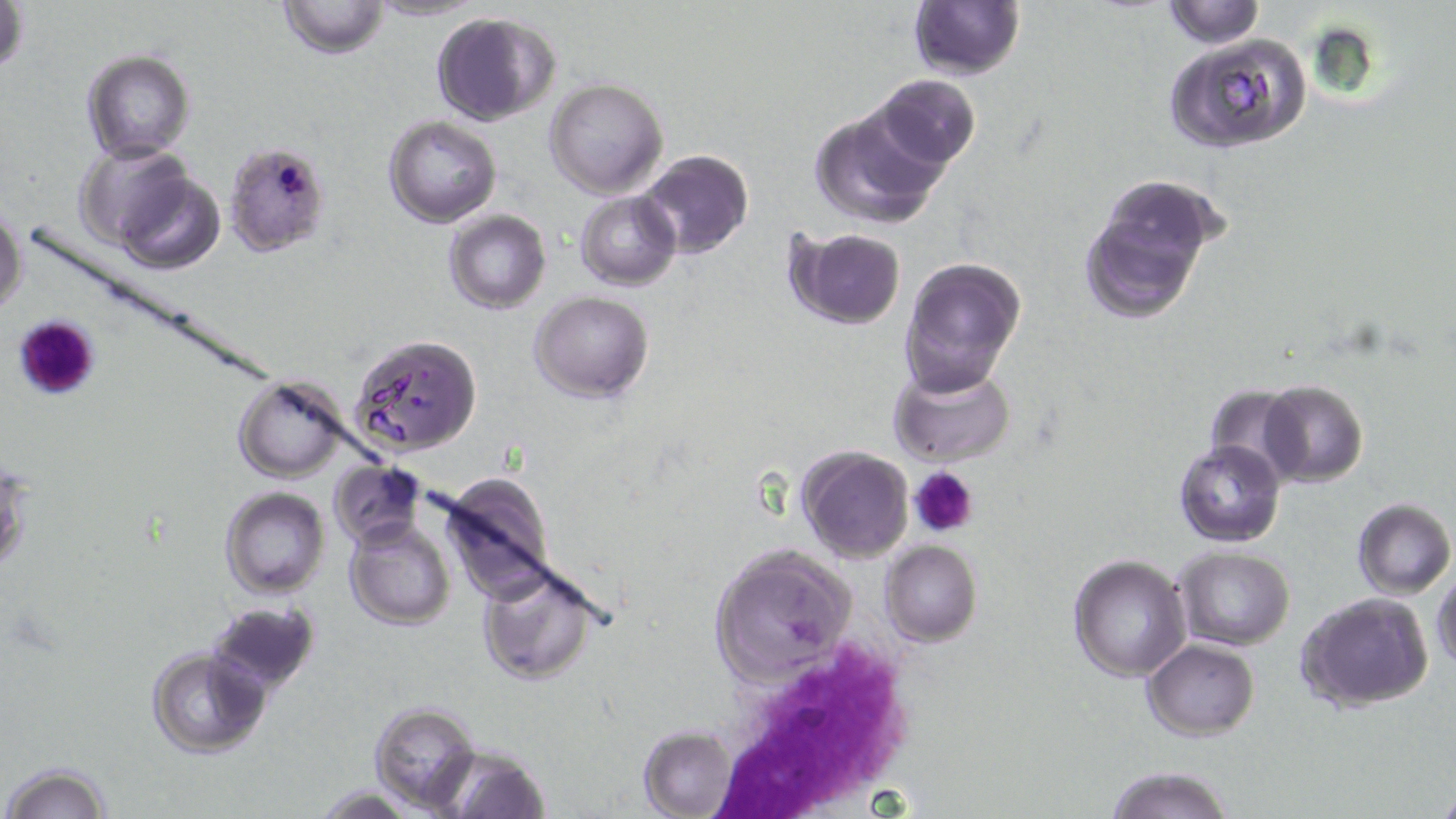
slide-level diagnosis = Plasmodium falciparum
preparation = thin blood film
white blood cell locations = approximate bounding boxes as (x1, y1, x2, y2) in pixels: (706, 636, 918, 818)
modality = light microscopy
platelet locations = approximate bounding boxes as (x1, y1, x2, y2) in pixels: (18, 314, 102, 400), (908, 466, 980, 539)
stain = May-Grünwald-Giemsa
uninfected red blood cell locations = approximate bounding boxes as (x1, y1, x2, y2) in pixels: (1, 0, 29, 80), (278, 0, 390, 59), (366, 0, 483, 22), (1161, 1, 1265, 50), (907, 3, 1026, 81), (432, 13, 559, 124), (1163, 32, 1313, 155), (82, 50, 195, 161), (870, 74, 982, 170), (544, 78, 669, 199), (808, 101, 953, 231), (383, 116, 501, 226), (74, 144, 197, 252), (637, 148, 754, 261), (108, 158, 225, 275), (1081, 178, 1222, 325), (576, 190, 680, 290), (0, 202, 27, 321), (444, 209, 550, 314), (784, 227, 908, 331), (898, 257, 1026, 399), (531, 290, 653, 402), (349, 335, 480, 456), (889, 362, 1017, 467), (233, 376, 352, 482), (1259, 380, 1368, 487), (1203, 383, 1306, 482), (1174, 439, 1285, 548), (797, 446, 915, 563), (329, 460, 425, 548), (437, 474, 558, 603), (220, 487, 331, 599), (1353, 498, 1455, 599), (345, 515, 458, 632), (880, 540, 982, 647), (707, 545, 856, 683), (1175, 546, 1295, 651), (1068, 555, 1191, 682), (476, 561, 601, 687), (1432, 570, 1456, 676), (1295, 591, 1435, 711), (206, 600, 321, 694), (1143, 639, 1258, 741), (146, 645, 270, 758), (368, 701, 481, 812), (636, 723, 742, 819), (436, 742, 551, 818), (2, 761, 112, 819), (1103, 764, 1236, 819)
image size = 1456×819 pixels
magnification = 1000x
field of view = single
Plasmodium falciparum-infected red blood cell locations = approximate bounding boxes as (x1, y1, x2, y2) in pixels: (223, 141, 332, 259)